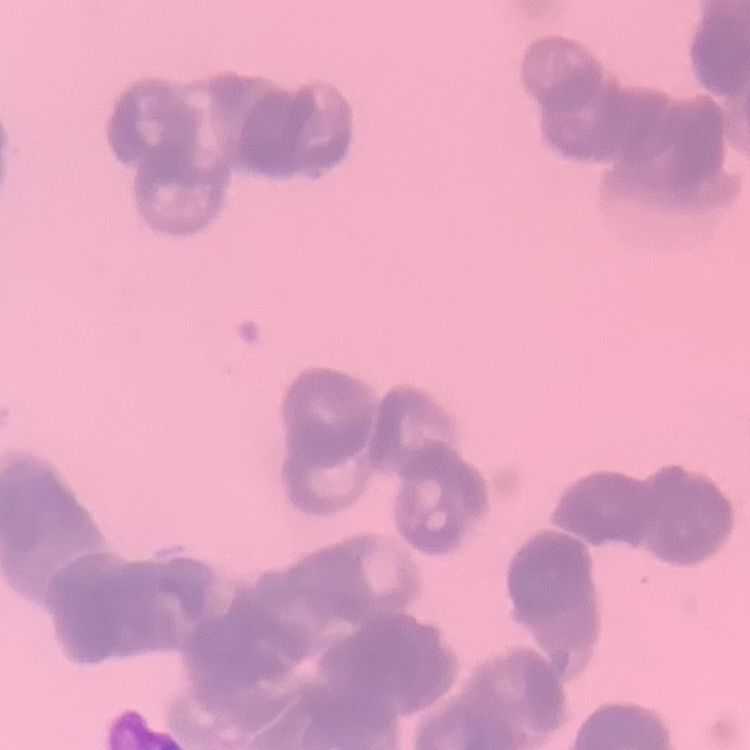

Summary:
  - Erythrocyte morphology: rouleaux formation
  - Image type: one tile cut from a larger photomicrograph
  - Stain: Field's or Giemsa
  - Preparation: thin peripheral smear